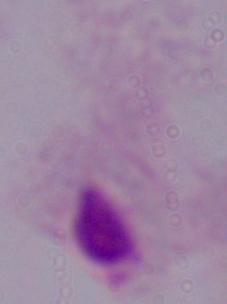
identification = trichomonad
modality = photomicrograph
magnification = 1000x